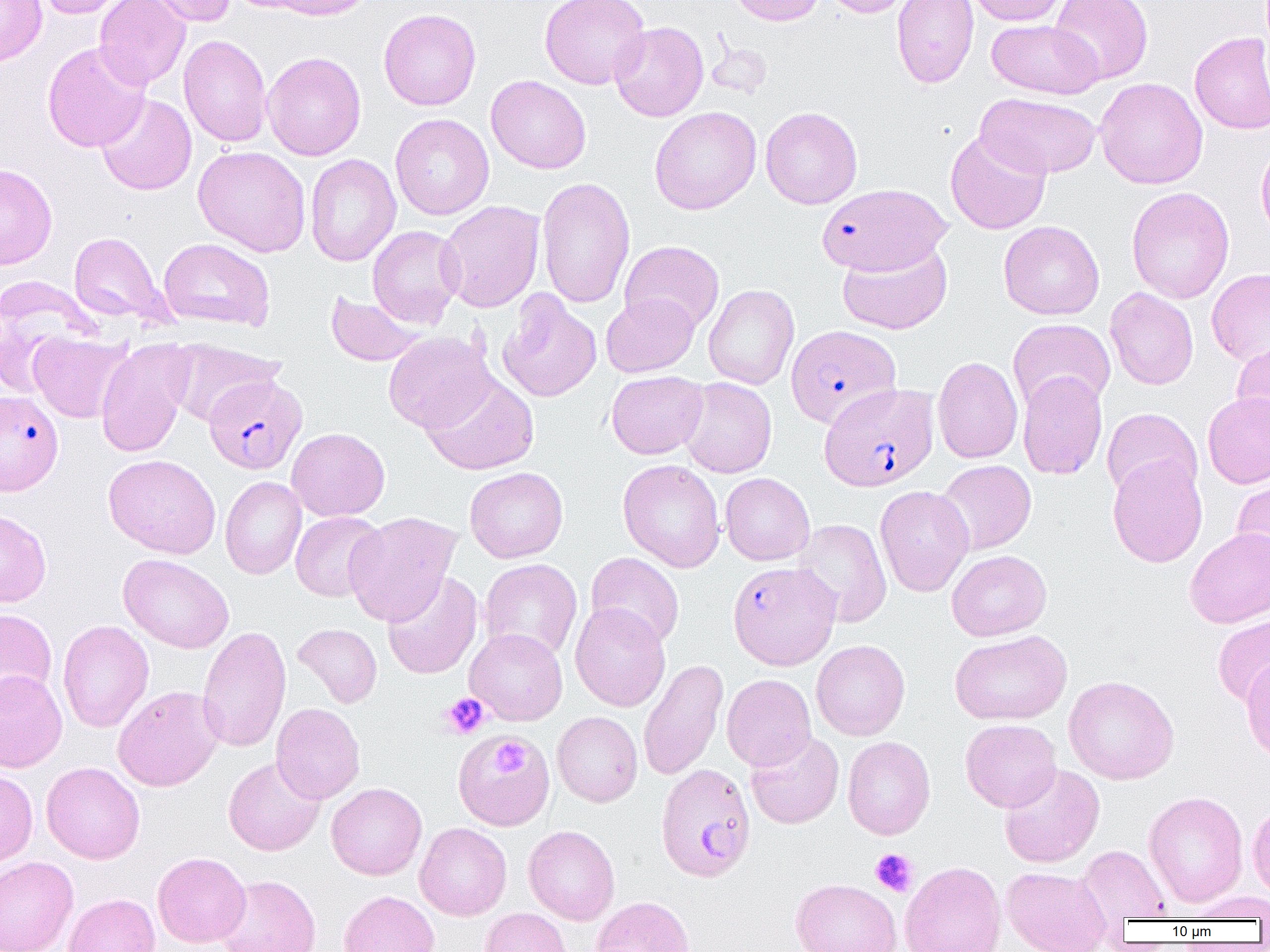

slide_level_diagnosis: Plasmodium falciparum
field_of_view: one of a larger specimen
modality: optical microscopy
image_size: 1270×952 pixels
plasmodium_falciparum_infected_red_blood_cell_locations_subset: 'approximate bounding boxes as named x1/y1/x2/y2 corners in pixels: (x1=817, y1=184, x2=951, y2=276), (x1=786, y1=325, x2=901, y2=428), (x1=203, y1=374, x2=307, y2=474), (x1=819, y1=383, x2=938, y2=491), (x1=0, y1=389, x2=63, y2=494), (x1=656, y1=763, x2=756, y2=881)'
platelet_locations_subset: 'approximate bounding boxes as named x1/y1/x2/y2 corners in pixels: (x1=441, y1=693, x2=490, y2=739), (x1=492, y1=739, x2=527, y2=778), (x1=870, y1=848, x2=918, y2=897)'
uninfected_red_blood_cell_locations_subset: 'approximate bounding boxes as named x1/y1/x2/y2 corners in pixels: (x1=0, y1=0, x2=47, y2=67), (x1=33, y1=0, x2=131, y2=18), (x1=94, y1=0, x2=190, y2=90), (x1=144, y1=0, x2=236, y2=27), (x1=225, y1=0, x2=322, y2=13), (x1=266, y1=0, x2=376, y2=20), (x1=540, y1=0, x2=650, y2=89), (x1=725, y1=0, x2=825, y2=26), (x1=822, y1=0, x2=915, y2=17), (x1=892, y1=0, x2=979, y2=89), (x1=965, y1=0, x2=1068, y2=26), (x1=1049, y1=0, x2=1153, y2=83), (x1=378, y1=8, x2=481, y2=110), (x1=986, y1=19, x2=1104, y2=99), (x1=609, y1=21, x2=709, y2=122), (x1=1189, y1=32, x2=1270, y2=135), (x1=178, y1=34, x2=272, y2=147), (x1=706, y1=36, x2=774, y2=98), (x1=42, y1=42, x2=151, y2=152), (x1=262, y1=52, x2=366, y2=160), (x1=486, y1=75, x2=591, y2=174), (x1=1095, y1=77, x2=1208, y2=189), (x1=96, y1=93, x2=197, y2=195), (x1=976, y1=93, x2=1102, y2=178), (x1=650, y1=106, x2=761, y2=214), (x1=760, y1=106, x2=863, y2=209), (x1=390, y1=113, x2=494, y2=220), (x1=945, y1=129, x2=1052, y2=234), (x1=1256, y1=139, x2=1270, y2=245), (x1=193, y1=145, x2=311, y2=257), (x1=305, y1=154, x2=401, y2=266), (x1=0, y1=163, x2=58, y2=269), (x1=536, y1=176, x2=635, y2=309), (x1=1126, y1=187, x2=1235, y2=303), (x1=437, y1=201, x2=545, y2=312), (x1=998, y1=220, x2=1104, y2=320), (x1=367, y1=225, x2=465, y2=328), (x1=69, y1=231, x2=172, y2=327), (x1=159, y1=238, x2=275, y2=330), (x1=619, y1=240, x2=725, y2=334), (x1=837, y1=240, x2=952, y2=335), (x1=1206, y1=269, x2=1270, y2=364), (x1=0, y1=277, x2=98, y2=395), (x1=703, y1=284, x2=799, y2=390), (x1=1105, y1=287, x2=1199, y2=390), (x1=325, y1=291, x2=428, y2=367), (x1=497, y1=291, x2=601, y2=403), (x1=601, y1=293, x2=699, y2=377), (x1=1008, y1=318, x2=1115, y2=413), (x1=383, y1=331, x2=496, y2=433), (x1=28, y1=332, x2=132, y2=423), (x1=167, y1=340, x2=286, y2=427), (x1=95, y1=341, x2=193, y2=458), (x1=1232, y1=341, x2=1270, y2=437), (x1=932, y1=355, x2=1023, y2=464), (x1=606, y1=370, x2=708, y2=459), (x1=1017, y1=371, x2=1107, y2=480), (x1=421, y1=373, x2=540, y2=476), (x1=678, y1=377, x2=777, y2=478), (x1=1202, y1=392, x2=1270, y2=489), (x1=1102, y1=408, x2=1202, y2=500), (x1=286, y1=427, x2=390, y2=521), (x1=103, y1=454, x2=221, y2=558), (x1=1107, y1=455, x2=1208, y2=568), (x1=618, y1=459, x2=725, y2=572), (x1=935, y1=459, x2=1036, y2=555), (x1=464, y1=467, x2=568, y2=563), (x1=720, y1=472, x2=815, y2=565), (x1=1231, y1=472, x2=1270, y2=576), (x1=220, y1=476, x2=307, y2=580), (x1=875, y1=485, x2=974, y2=596), (x1=0, y1=510, x2=52, y2=607), (x1=290, y1=511, x2=386, y2=602), (x1=343, y1=512, x2=461, y2=626), (x1=793, y1=518, x2=892, y2=627), (x1=1185, y1=528, x2=1270, y2=628), (x1=946, y1=549, x2=1051, y2=641), (x1=585, y1=552, x2=684, y2=649), (x1=118, y1=553, x2=234, y2=652), (x1=479, y1=558, x2=582, y2=661), (x1=382, y1=571, x2=483, y2=679), (x1=570, y1=603, x2=670, y2=711), (x1=0, y1=608, x2=57, y2=707), (x1=1213, y1=614, x2=1270, y2=707), (x1=57, y1=620, x2=154, y2=732), (x1=292, y1=623, x2=382, y2=707), (x1=197, y1=625, x2=291, y2=753), (x1=465, y1=627, x2=568, y2=725), (x1=950, y1=629, x2=1072, y2=725), (x1=812, y1=640, x2=910, y2=740), (x1=1241, y1=657, x2=1270, y2=760), (x1=638, y1=658, x2=729, y2=781), (x1=0, y1=669, x2=67, y2=772), (x1=721, y1=674, x2=816, y2=770), (x1=1063, y1=675, x2=1179, y2=785), (x1=112, y1=685, x2=224, y2=791), (x1=271, y1=702, x2=365, y2=804), (x1=552, y1=711, x2=642, y2=807), (x1=960, y1=719, x2=1061, y2=812), (x1=745, y1=731, x2=844, y2=829), (x1=843, y1=736, x2=935, y2=839), (x1=223, y1=756, x2=325, y2=856), (x1=41, y1=761, x2=145, y2=864), (x1=998, y1=763, x2=1104, y2=868), (x1=0, y1=770, x2=38, y2=868), (x1=326, y1=782, x2=427, y2=880), (x1=1144, y1=791, x2=1249, y2=908), (x1=1247, y1=801, x2=1270, y2=901), (x1=414, y1=822, x2=512, y2=920), (x1=523, y1=825, x2=620, y2=925), (x1=1077, y1=845, x2=1169, y2=922), (x1=153, y1=851, x2=251, y2=948), (x1=0, y1=856, x2=78, y2=952), (x1=899, y1=860, x2=1006, y2=952), (x1=1001, y1=866, x2=1112, y2=952), (x1=215, y1=875, x2=321, y2=952), (x1=790, y1=878, x2=902, y2=952), (x1=339, y1=890, x2=440, y2=952), (x1=1186, y1=891, x2=1270, y2=921), (x1=63, y1=893, x2=161, y2=952), (x1=591, y1=896, x2=695, y2=952), (x1=479, y1=908, x2=571, y2=952)'
magnification: 1000x
preparation: thin blood smear